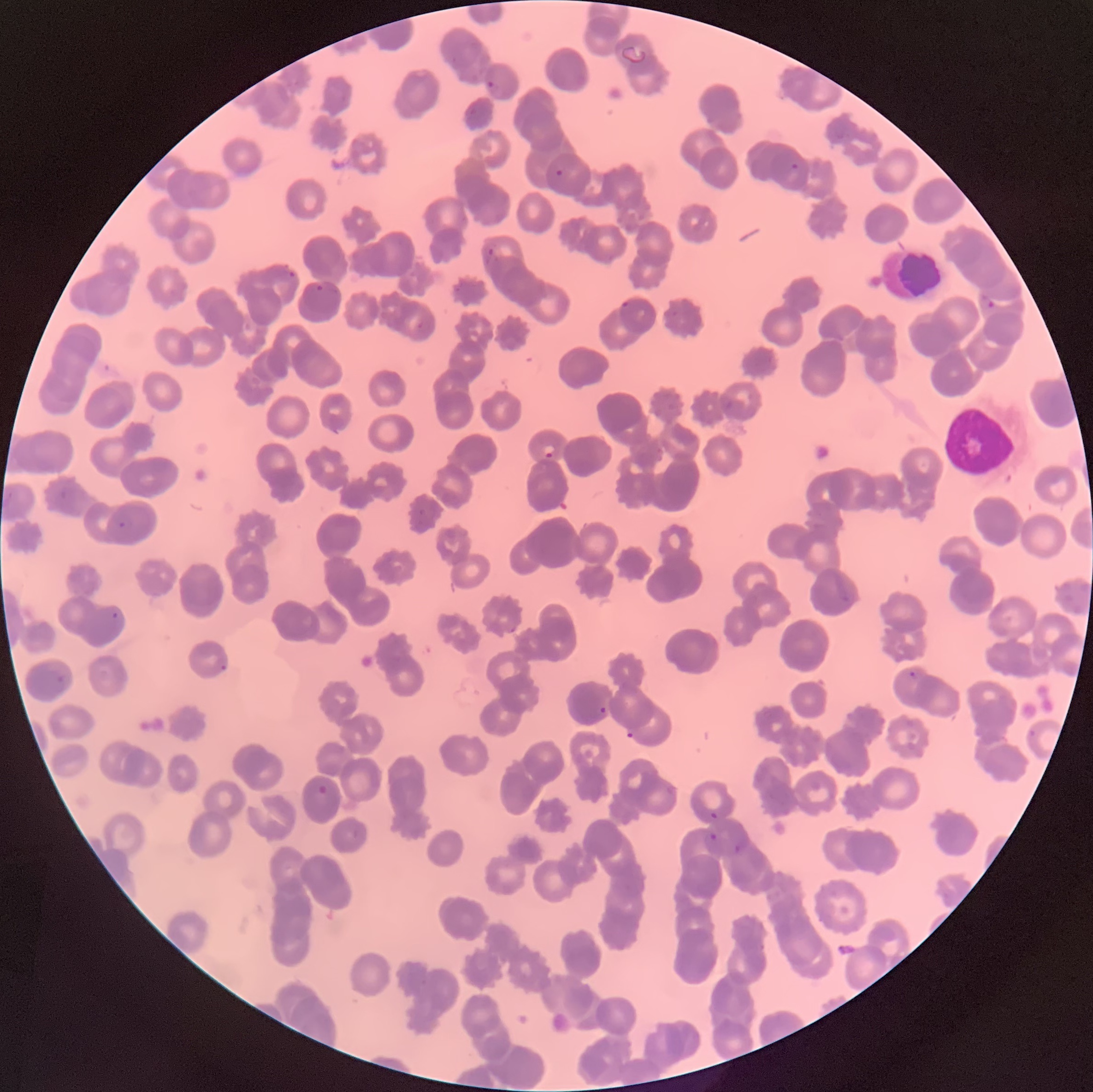
coordinate format = approximate bounding boxes as (x1, y1, x2, y2) in pixels
white blood cell locations = (944, 404, 1018, 482)
Plasmodium parasite locations = (488, 80, 502, 97), (789, 162, 799, 171), (554, 168, 565, 177), (485, 247, 498, 266), (273, 270, 295, 284), (314, 283, 324, 293), (979, 295, 995, 311), (621, 300, 629, 309), (416, 320, 424, 330), (720, 392, 733, 412), (542, 444, 556, 459), (56, 490, 71, 505), (5, 491, 16, 507), (117, 515, 133, 529), (111, 611, 120, 620), (220, 664, 228, 672), (908, 670, 917, 679), (55, 673, 65, 685), (599, 706, 607, 714), (625, 730, 636, 740), (317, 784, 328, 794), (709, 810, 718, 820), (703, 832, 718, 842), (735, 842, 748, 856)
preparation = thin blood smear
image size = 1093×1092 pixels
modality = light microscopy
red blood cell morphology = rouleaux formation